Outline platelets.
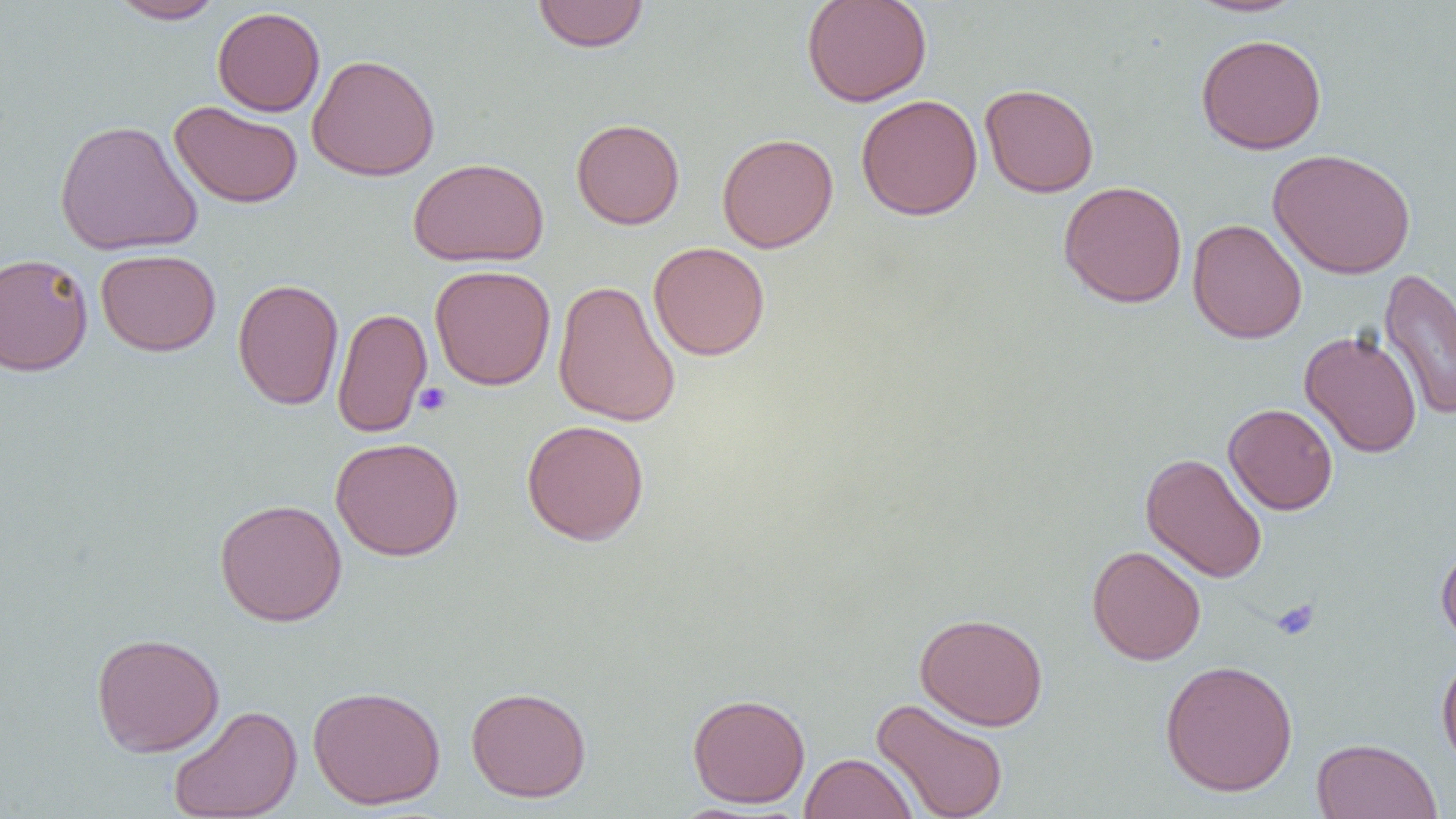
Approximate bounding boxes as (x1, y1, x2, y2) in pixels.
Platelets: (413, 383, 452, 417), (1271, 597, 1321, 641).

Uninfected red blood cell locations: (108, 0, 227, 24), (532, 0, 649, 53), (801, 0, 932, 108), (1184, 0, 1309, 18), (212, 6, 326, 116), (1195, 33, 1327, 154), (306, 53, 440, 181), (979, 83, 1099, 198), (856, 94, 983, 220), (169, 100, 303, 209), (54, 118, 203, 256), (571, 118, 685, 229), (716, 133, 839, 253), (1268, 148, 1416, 279), (407, 157, 549, 267), (1058, 181, 1188, 308), (1187, 218, 1307, 344), (648, 241, 771, 360), (95, 249, 221, 356), (0, 252, 94, 376), (430, 264, 556, 391), (1378, 267, 1456, 421), (232, 278, 344, 410), (553, 280, 681, 427), (332, 307, 432, 438), (1299, 329, 1423, 458), (1224, 403, 1338, 515), (521, 419, 650, 545), (330, 436, 464, 561), (1140, 452, 1267, 583), (214, 498, 347, 626), (1436, 538, 1456, 650), (1086, 545, 1206, 665), (914, 612, 1049, 731), (91, 632, 225, 757), (1436, 651, 1456, 773), (1159, 659, 1298, 797), (307, 685, 446, 810), (466, 685, 592, 802), (687, 692, 811, 808), (871, 697, 1010, 819), (168, 704, 302, 818), (1311, 738, 1443, 819), (800, 752, 918, 819). Slide-level diagnosis: negative for blood parasites. One field of a larger specimen. Captured at 1000x magnification. Light microscopy. Thin blood film. Image is 1456×819 pixels.